State which cell type is depicted.
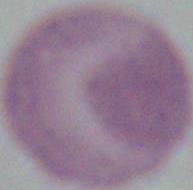

This is an erythrocyte.

magnification = 1000x
modality = micrograph